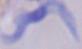

Summary:
  - Modality: micrograph
  - Magnification: 1000x
  - Identification: trypanosome